Comment on the morphology of the erythrocytes.
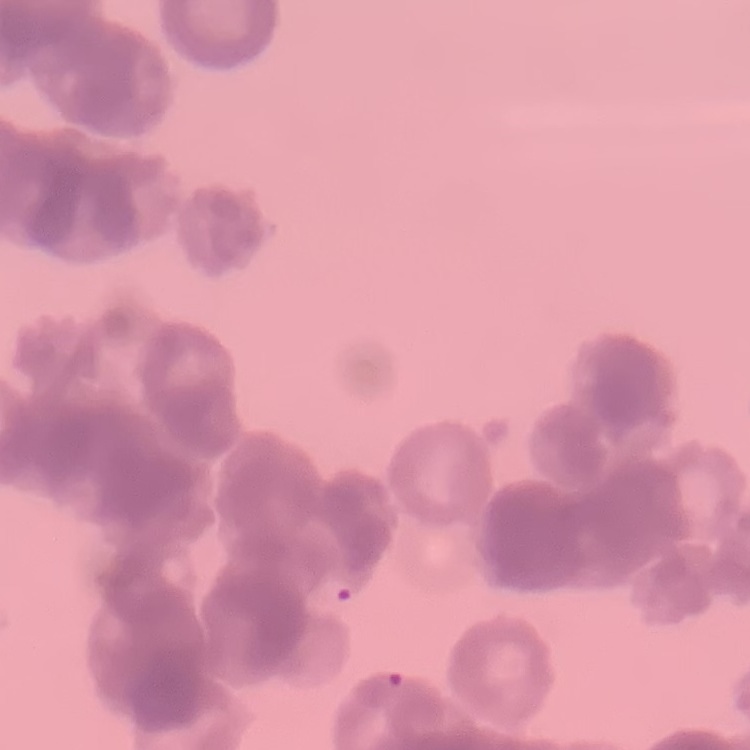

Rouleaux formation.

image type = one tile cut from a larger photomicrograph
stain = Field's or Giemsa
preparation = thin blood smear